Describe the morphology of the erythrocytes.
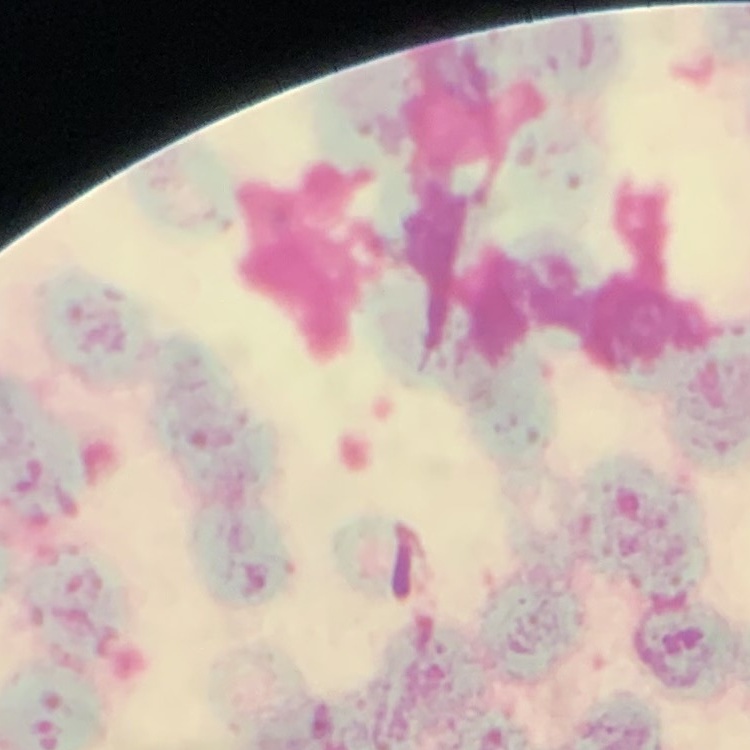
They show rouleaux formation.

preparation = thin blood film
stain = Field's or Giemsa
image type = square crop of a larger photomicrograph